Outline each blood parasite and name the species.
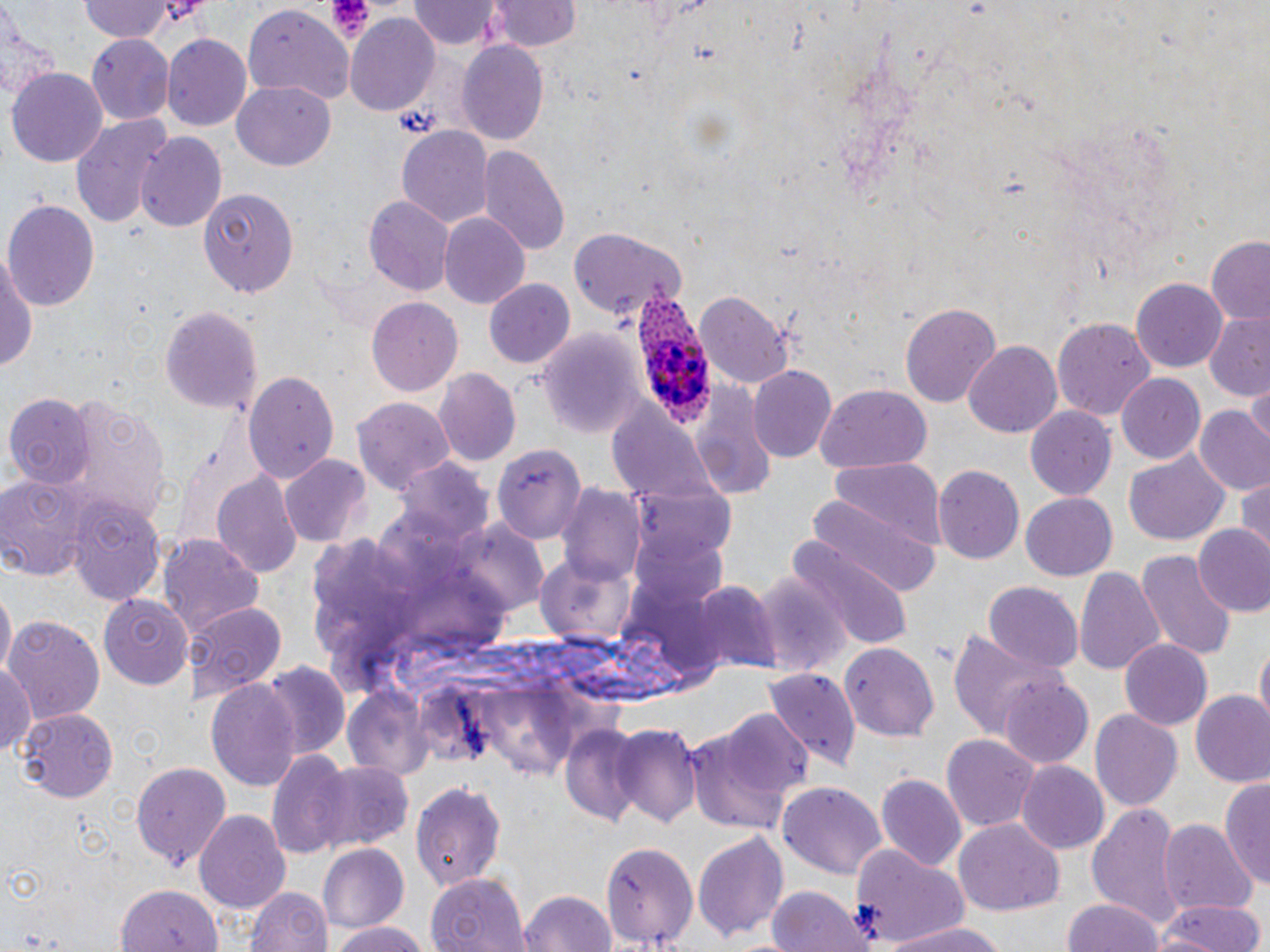

Approximate bounding boxes as named x1/y1/x2/y2 corners in pixels.
Plasmodium ovale-infected red blood cells: (x1=632, y1=277, x2=718, y2=428).
No Plasmodium falciparum, Plasmodium malariae, Plasmodium vivax, Babesia divergens, or Trypanosoma brucei observed.

Summary:
  - Platelet locations: (x1=153, y1=0, x2=210, y2=33), (x1=325, y1=0, x2=374, y2=42)
  - Uninfected red blood cell locations: (x1=410, y1=0, x2=500, y2=50), (x1=490, y1=0, x2=581, y2=54), (x1=76, y1=1, x2=179, y2=43), (x1=241, y1=5, x2=353, y2=103), (x1=0, y1=7, x2=58, y2=104), (x1=343, y1=17, x2=440, y2=113), (x1=86, y1=31, x2=175, y2=123), (x1=161, y1=35, x2=252, y2=130), (x1=457, y1=41, x2=549, y2=148), (x1=8, y1=69, x2=107, y2=168), (x1=231, y1=80, x2=335, y2=172), (x1=69, y1=112, x2=175, y2=226), (x1=396, y1=124, x2=494, y2=231), (x1=136, y1=133, x2=226, y2=234), (x1=477, y1=143, x2=569, y2=255), (x1=200, y1=186, x2=299, y2=296), (x1=365, y1=194, x2=452, y2=298), (x1=4, y1=198, x2=98, y2=309), (x1=439, y1=214, x2=530, y2=310), (x1=570, y1=228, x2=687, y2=321), (x1=1207, y1=238, x2=1270, y2=324), (x1=0, y1=247, x2=39, y2=382), (x1=1133, y1=279, x2=1229, y2=373), (x1=485, y1=280, x2=576, y2=371), (x1=695, y1=291, x2=795, y2=385), (x1=364, y1=297, x2=463, y2=396), (x1=899, y1=301, x2=1003, y2=407), (x1=161, y1=302, x2=263, y2=418), (x1=1204, y1=314, x2=1270, y2=402), (x1=1053, y1=318, x2=1155, y2=419), (x1=538, y1=328, x2=649, y2=439), (x1=963, y1=342, x2=1064, y2=438), (x1=747, y1=365, x2=837, y2=462), (x1=243, y1=367, x2=339, y2=485), (x1=434, y1=369, x2=521, y2=467), (x1=1119, y1=373, x2=1205, y2=464), (x1=686, y1=378, x2=775, y2=499), (x1=1246, y1=380, x2=1269, y2=448), (x1=815, y1=386, x2=932, y2=470), (x1=62, y1=392, x2=171, y2=526), (x1=6, y1=395, x2=94, y2=487), (x1=355, y1=396, x2=454, y2=494), (x1=608, y1=404, x2=713, y2=505), (x1=1195, y1=406, x2=1270, y2=497), (x1=1025, y1=408, x2=1116, y2=502), (x1=491, y1=441, x2=586, y2=545), (x1=1123, y1=450, x2=1231, y2=546), (x1=280, y1=455, x2=371, y2=547), (x1=827, y1=456, x2=944, y2=550), (x1=396, y1=460, x2=497, y2=546), (x1=931, y1=464, x2=1023, y2=564), (x1=0, y1=472, x2=102, y2=581), (x1=214, y1=472, x2=299, y2=576), (x1=1236, y1=475, x2=1270, y2=552), (x1=629, y1=481, x2=739, y2=579), (x1=558, y1=485, x2=646, y2=586), (x1=1021, y1=493, x2=1117, y2=580), (x1=67, y1=497, x2=166, y2=607), (x1=802, y1=498, x2=942, y2=598), (x1=1192, y1=524, x2=1270, y2=615), (x1=158, y1=534, x2=262, y2=637), (x1=786, y1=541, x2=912, y2=657), (x1=1134, y1=548, x2=1234, y2=660), (x1=534, y1=549, x2=637, y2=647), (x1=1073, y1=566, x2=1164, y2=677), (x1=750, y1=572, x2=845, y2=676), (x1=692, y1=582, x2=780, y2=675), (x1=983, y1=582, x2=1083, y2=673), (x1=2, y1=591, x2=15, y2=674), (x1=99, y1=594, x2=194, y2=688), (x1=184, y1=602, x2=285, y2=705), (x1=5, y1=615, x2=105, y2=724), (x1=945, y1=630, x2=1057, y2=740), (x1=1120, y1=638, x2=1213, y2=730), (x1=1256, y1=640, x2=1269, y2=725), (x1=839, y1=642, x2=940, y2=742), (x1=0, y1=660, x2=38, y2=760), (x1=262, y1=664, x2=349, y2=758), (x1=765, y1=668, x2=861, y2=772), (x1=999, y1=676, x2=1093, y2=769), (x1=205, y1=679, x2=302, y2=789), (x1=1190, y1=692, x2=1270, y2=788), (x1=687, y1=706, x2=812, y2=835), (x1=14, y1=708, x2=119, y2=803), (x1=1089, y1=708, x2=1181, y2=809), (x1=613, y1=724, x2=705, y2=828), (x1=561, y1=726, x2=644, y2=826), (x1=941, y1=732, x2=1038, y2=833), (x1=266, y1=752, x2=354, y2=860), (x1=131, y1=760, x2=231, y2=869), (x1=304, y1=763, x2=413, y2=853), (x1=1017, y1=763, x2=1108, y2=852), (x1=877, y1=774, x2=967, y2=871), (x1=1222, y1=778, x2=1270, y2=890), (x1=412, y1=779, x2=507, y2=893), (x1=778, y1=779, x2=887, y2=878), (x1=1089, y1=800, x2=1182, y2=928), (x1=195, y1=809, x2=291, y2=911), (x1=955, y1=819, x2=1064, y2=918), (x1=1158, y1=820, x2=1255, y2=917), (x1=693, y1=826, x2=788, y2=942), (x1=599, y1=838, x2=697, y2=951), (x1=849, y1=842, x2=972, y2=947), (x1=320, y1=846, x2=412, y2=935), (x1=425, y1=874, x2=528, y2=952), (x1=118, y1=881, x2=222, y2=952), (x1=244, y1=884, x2=333, y2=952), (x1=767, y1=885, x2=869, y2=952), (x1=516, y1=889, x2=617, y2=952), (x1=1065, y1=897, x2=1166, y2=952), (x1=1159, y1=899, x2=1266, y2=952), (x1=325, y1=921, x2=435, y2=952), (x1=884, y1=921, x2=1015, y2=952)
  - Slide-level diagnosis: Plasmodium ovale
  - Magnification: 1000x
  - Stain: May-Grünwald-Giemsa
  - Modality: optical microscopy
  - Image size: 1270×952 pixels
  - Preparation: thin blood smear
  - Field of view: single